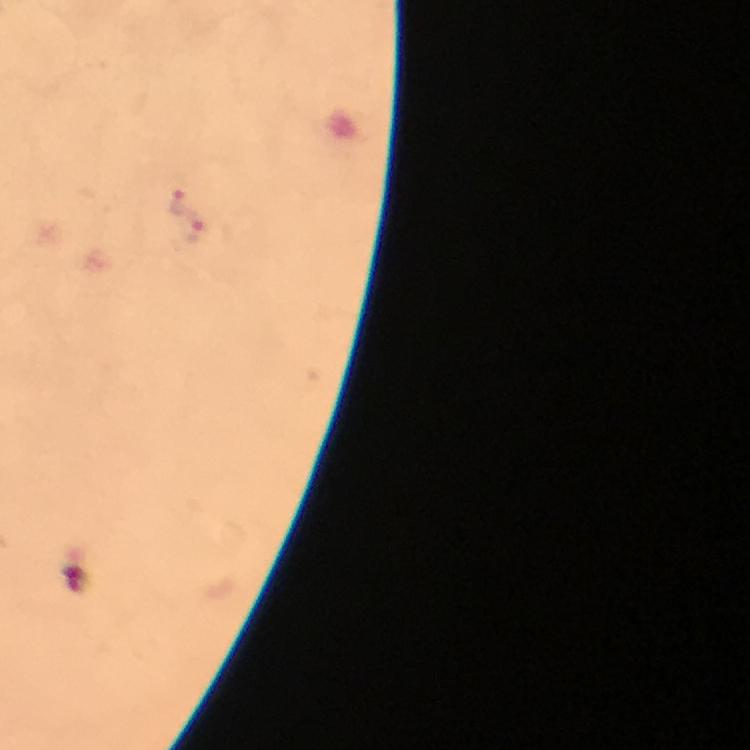
immersion oil = used
context = from a diagnostic examination for malaria
image size = 750×750 pixels
cropped from = a single field of view
magnification = 100x
Plasmodium parasite locations = approximate centers as [x, y] in pixels: [180, 198], [191, 229]
stain = Giemsa
preparation = thick blood smear
capture = smartphone photograph through a microscope